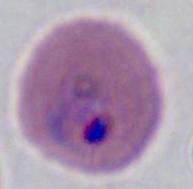
A Plasmodium parasite is shown. Captured at either 400x or 1000x magnification. Photomicrograph.